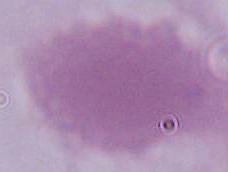

modality = micrograph
magnification = 1000x
identification = erythrocyte